Outline each Trypanosoma brucei.
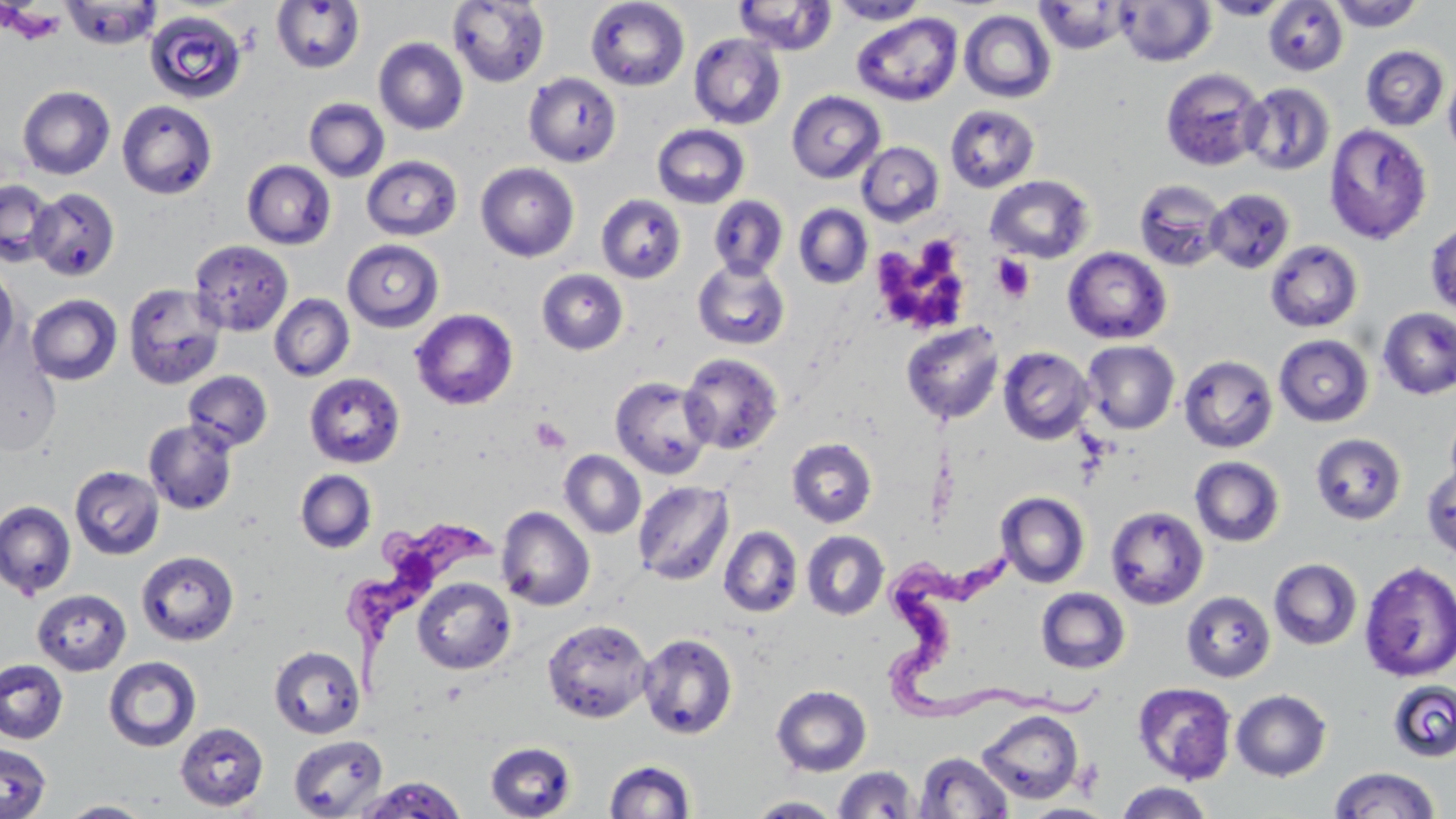
Approximate bounding boxes as named x1/y1/x2/y2 corners in pixels.
Trypanosoma brucei: (x1=343, y1=515, x2=513, y2=684), (x1=879, y1=553, x2=1117, y2=719).

{
  "slide_level_diagnosis": "Trypanosoma brucei",
  "platelet_locations": "approximate bounding boxes as named x1/y1/x2/y2 corners in pixels: (x1=4, y1=5, x2=67, y2=44), (x1=870, y1=234, x2=974, y2=335), (x1=991, y1=254, x2=1036, y2=303), (x1=530, y1=417, x2=570, y2=454)",
  "field_of_view": "one of a larger specimen",
  "preparation": "thin blood smear",
  "modality": "optical microscopy",
  "uninfected_red_blood_cell_locations": "approximate bounding boxes as named x1/y1/x2/y2 corners in pixels: (x1=447, y1=0, x2=549, y2=87), (x1=585, y1=0, x2=690, y2=91), (x1=733, y1=0, x2=837, y2=56), (x1=1204, y1=0, x2=1291, y2=20), (x1=61, y1=1, x2=163, y2=49), (x1=271, y1=1, x2=365, y2=74), (x1=829, y1=1, x2=929, y2=25), (x1=1034, y1=1, x2=1134, y2=54), (x1=1116, y1=1, x2=1216, y2=67), (x1=1263, y1=1, x2=1348, y2=76), (x1=1328, y1=1, x2=1425, y2=31), (x1=144, y1=10, x2=248, y2=104), (x1=959, y1=10, x2=1056, y2=103), (x1=852, y1=13, x2=962, y2=105), (x1=689, y1=33, x2=786, y2=130), (x1=374, y1=37, x2=468, y2=135), (x1=1361, y1=45, x2=1450, y2=131), (x1=1443, y1=63, x2=1456, y2=159), (x1=1160, y1=67, x2=1268, y2=171), (x1=523, y1=72, x2=621, y2=167), (x1=1242, y1=82, x2=1335, y2=176), (x1=17, y1=85, x2=115, y2=180), (x1=786, y1=90, x2=886, y2=183), (x1=17, y1=93, x2=219, y2=184), (x1=304, y1=98, x2=390, y2=182), (x1=116, y1=100, x2=217, y2=199), (x1=945, y1=104, x2=1040, y2=193), (x1=652, y1=123, x2=750, y2=209), (x1=1323, y1=123, x2=1433, y2=245), (x1=857, y1=141, x2=944, y2=226), (x1=362, y1=155, x2=462, y2=240), (x1=242, y1=160, x2=336, y2=249), (x1=475, y1=162, x2=579, y2=262), (x1=985, y1=175, x2=1094, y2=263), (x1=1133, y1=178, x2=1229, y2=271), (x1=0, y1=180, x2=58, y2=267), (x1=29, y1=187, x2=120, y2=281), (x1=1206, y1=188, x2=1295, y2=274), (x1=596, y1=194, x2=686, y2=283), (x1=708, y1=195, x2=789, y2=279), (x1=793, y1=203, x2=873, y2=289), (x1=1425, y1=219, x2=1456, y2=319), (x1=189, y1=240, x2=293, y2=336), (x1=342, y1=240, x2=444, y2=332), (x1=1265, y1=240, x2=1363, y2=332), (x1=1063, y1=247, x2=1172, y2=345), (x1=692, y1=258, x2=790, y2=350), (x1=0, y1=263, x2=20, y2=362), (x1=537, y1=269, x2=629, y2=355), (x1=123, y1=282, x2=226, y2=390), (x1=26, y1=293, x2=123, y2=386), (x1=269, y1=294, x2=355, y2=382), (x1=1377, y1=307, x2=1456, y2=399), (x1=410, y1=309, x2=518, y2=411), (x1=900, y1=321, x2=1006, y2=425), (x1=1274, y1=334, x2=1374, y2=427), (x1=1081, y1=340, x2=1180, y2=434), (x1=0, y1=342, x2=62, y2=457), (x1=997, y1=346, x2=1096, y2=445), (x1=680, y1=353, x2=784, y2=454), (x1=1179, y1=354, x2=1278, y2=453), (x1=183, y1=370, x2=273, y2=452), (x1=304, y1=372, x2=405, y2=468), (x1=610, y1=376, x2=715, y2=479), (x1=1444, y1=406, x2=1456, y2=498), (x1=144, y1=419, x2=238, y2=514), (x1=1311, y1=433, x2=1407, y2=525), (x1=786, y1=437, x2=877, y2=528), (x1=560, y1=450, x2=646, y2=538), (x1=1189, y1=456, x2=1285, y2=547), (x1=1422, y1=464, x2=1456, y2=561), (x1=70, y1=465, x2=164, y2=560), (x1=294, y1=469, x2=377, y2=553), (x1=632, y1=481, x2=734, y2=585), (x1=997, y1=492, x2=1090, y2=588), (x1=0, y1=501, x2=75, y2=599), (x1=1105, y1=505, x2=1209, y2=609), (x1=496, y1=506, x2=595, y2=611), (x1=718, y1=526, x2=803, y2=617), (x1=802, y1=530, x2=890, y2=620), (x1=136, y1=549, x2=239, y2=647), (x1=1268, y1=558, x2=1363, y2=650), (x1=1359, y1=561, x2=1456, y2=682), (x1=413, y1=578, x2=515, y2=674), (x1=1035, y1=587, x2=1131, y2=673), (x1=32, y1=589, x2=131, y2=675), (x1=1181, y1=590, x2=1276, y2=682), (x1=542, y1=618, x2=654, y2=723), (x1=638, y1=632, x2=738, y2=739), (x1=269, y1=645, x2=365, y2=739), (x1=103, y1=656, x2=201, y2=752), (x1=0, y1=659, x2=68, y2=744), (x1=1387, y1=680, x2=1456, y2=763), (x1=1133, y1=682, x2=1236, y2=784), (x1=771, y1=685, x2=871, y2=776), (x1=1231, y1=689, x2=1331, y2=781), (x1=976, y1=709, x2=1084, y2=805), (x1=174, y1=722, x2=269, y2=812), (x1=288, y1=734, x2=388, y2=818), (x1=485, y1=741, x2=577, y2=819), (x1=1, y1=742, x2=52, y2=819), (x1=913, y1=751, x2=1014, y2=818), (x1=604, y1=759, x2=696, y2=818), (x1=832, y1=766, x2=920, y2=817), (x1=1328, y1=767, x2=1441, y2=817), (x1=356, y1=776, x2=467, y2=818), (x1=1114, y1=782, x2=1215, y2=819), (x1=748, y1=796, x2=842, y2=817), (x1=59, y1=800, x2=155, y2=817), (x1=1021, y1=804, x2=1116, y2=819)",
  "stain": "May-Grünwald-Giemsa",
  "magnification": "1000x",
  "image_size": "1456×819 pixels"
}